State the preparation type.
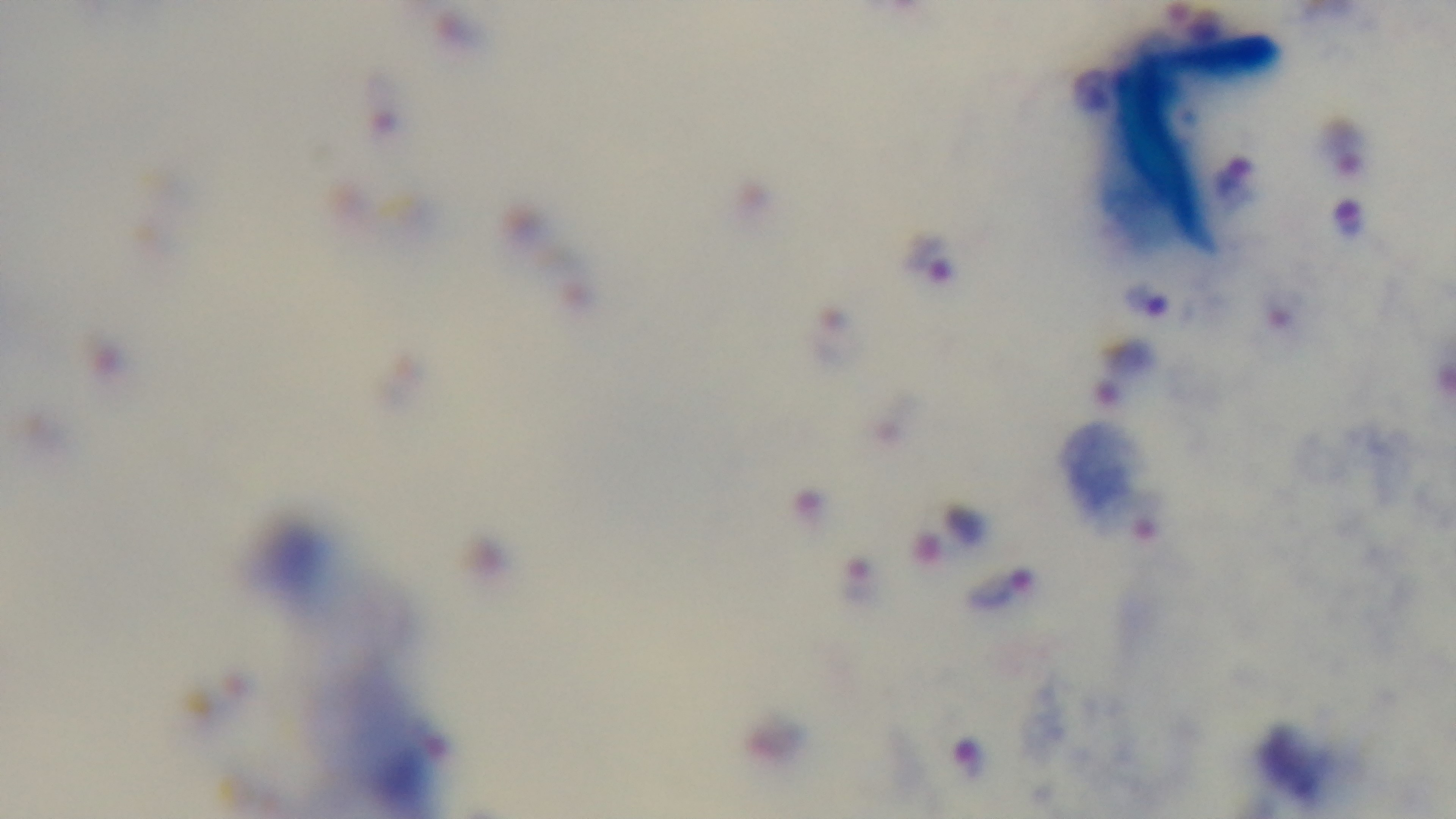

It is a thick blood film.

Malaria status: positive. Light microscopy. 100x oil-immersion objective. Giemsa-stained. Mounted 4K digital camera. One field from the slide.